Point out each leukocyte.
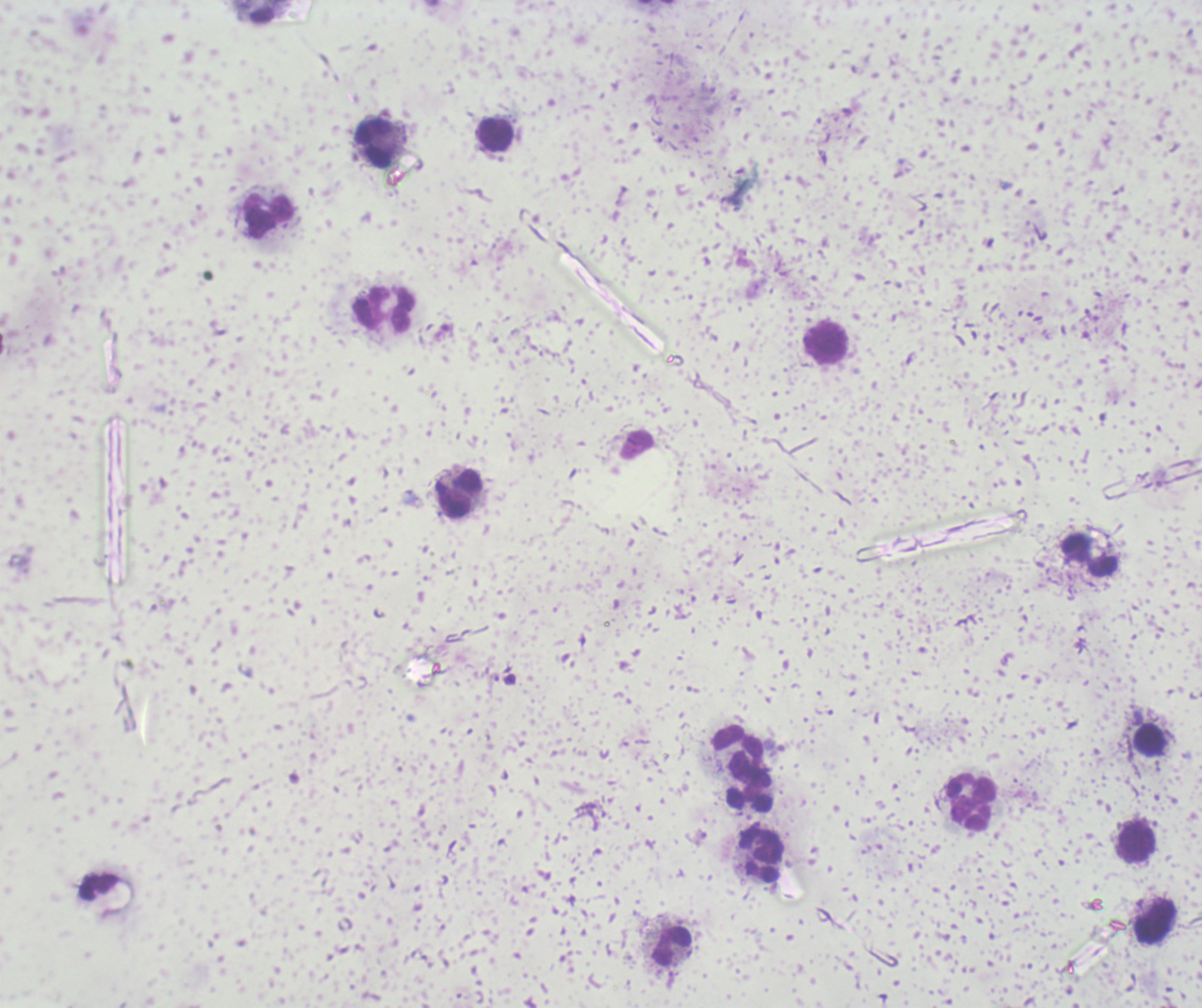
Approximate centers as [x, y] in pixels.
Leukocytes: [260, 11], [494, 135], [376, 143], [269, 216], [384, 308], [825, 342], [459, 493], [1090, 555], [1149, 739], [737, 745], [750, 785], [971, 802], [1136, 844], [761, 854], [1155, 922], [671, 947].

Result: negative for Plasmodium parasites. Romanowsky-stained preparation. Image is 1202×1008 pixels. Background quality: poor. Previously used in a real diagnosis. Thick blood smear. One field from this slide. Captured at 100x magnification.